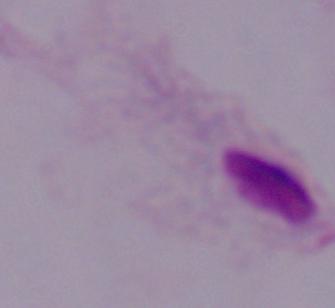
magnification = 1000x
identification = trichomonad
modality = micrograph